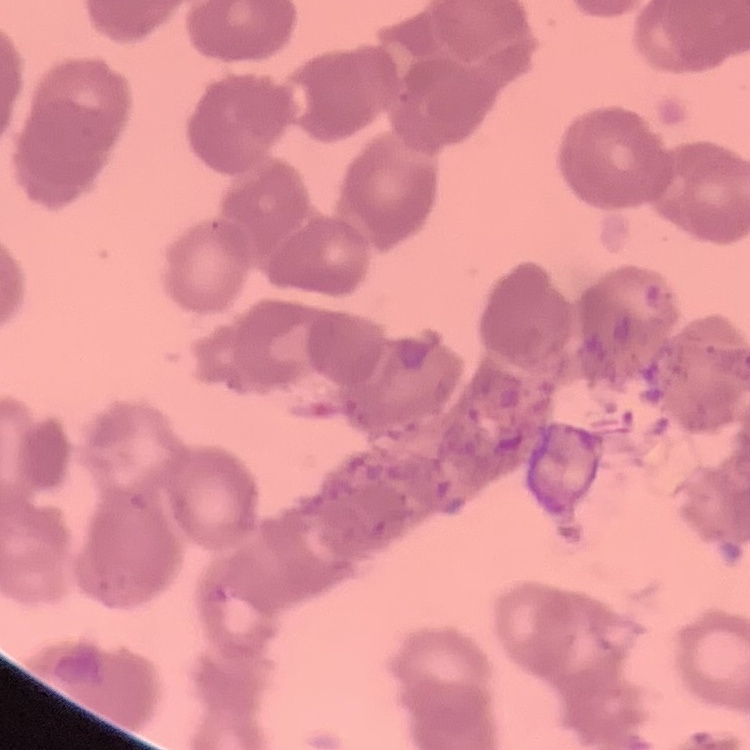
Summary:
  - Red blood cell morphology: rouleaux formation
  - Image type: square crop of a larger photomicrograph
  - Preparation: thin blood film
  - Stain: Field's or Giemsa